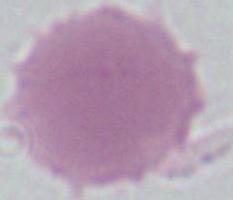 An erythrocyte is shown. Captured at 1000x magnification. Photomicrograph.